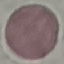 Malaria status: uninfected. Acquired by smartphone through the microscope eyepiece. Giemsa stain. Cell patch, automatically extracted from a larger field of view and resized to 64 × 64 pixels. Thin smear of blood.